Assess this cell for malaria.
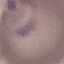

It is parasitized.

Summary:
  - Stain: Giemsa
  - Capture: smartphone through the microscope eyepiece
  - Preparation: thin blood film
  - Image type: cell patch, automatically extracted from a larger field of view and resized to 64 × 64 pixels